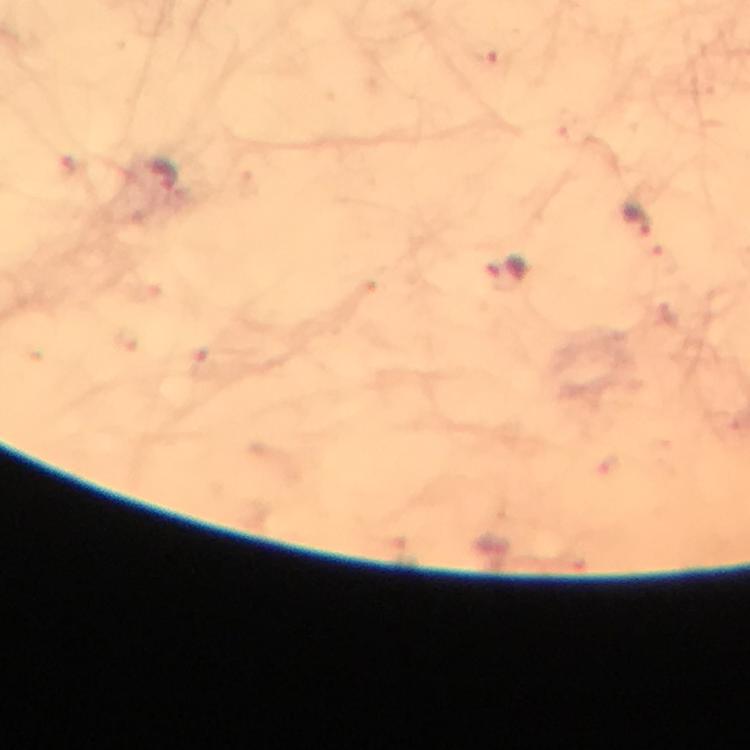
{
  "stain": "Giemsa",
  "cropped_from": "one field of view",
  "malaria_parasite_locations": "approximate centers as [x, y] in pixels: [160, 176], [638, 219], [507, 273]",
  "preparation": "thick blood smear",
  "context": "from a diagnostic examination for malaria",
  "magnification": "100x",
  "immersion_oil": "used",
  "image_size": "750×750 pixels",
  "capture": "smartphone camera through the microscope"
}